Outline each Plasmodium ovale-infected red blood cell.
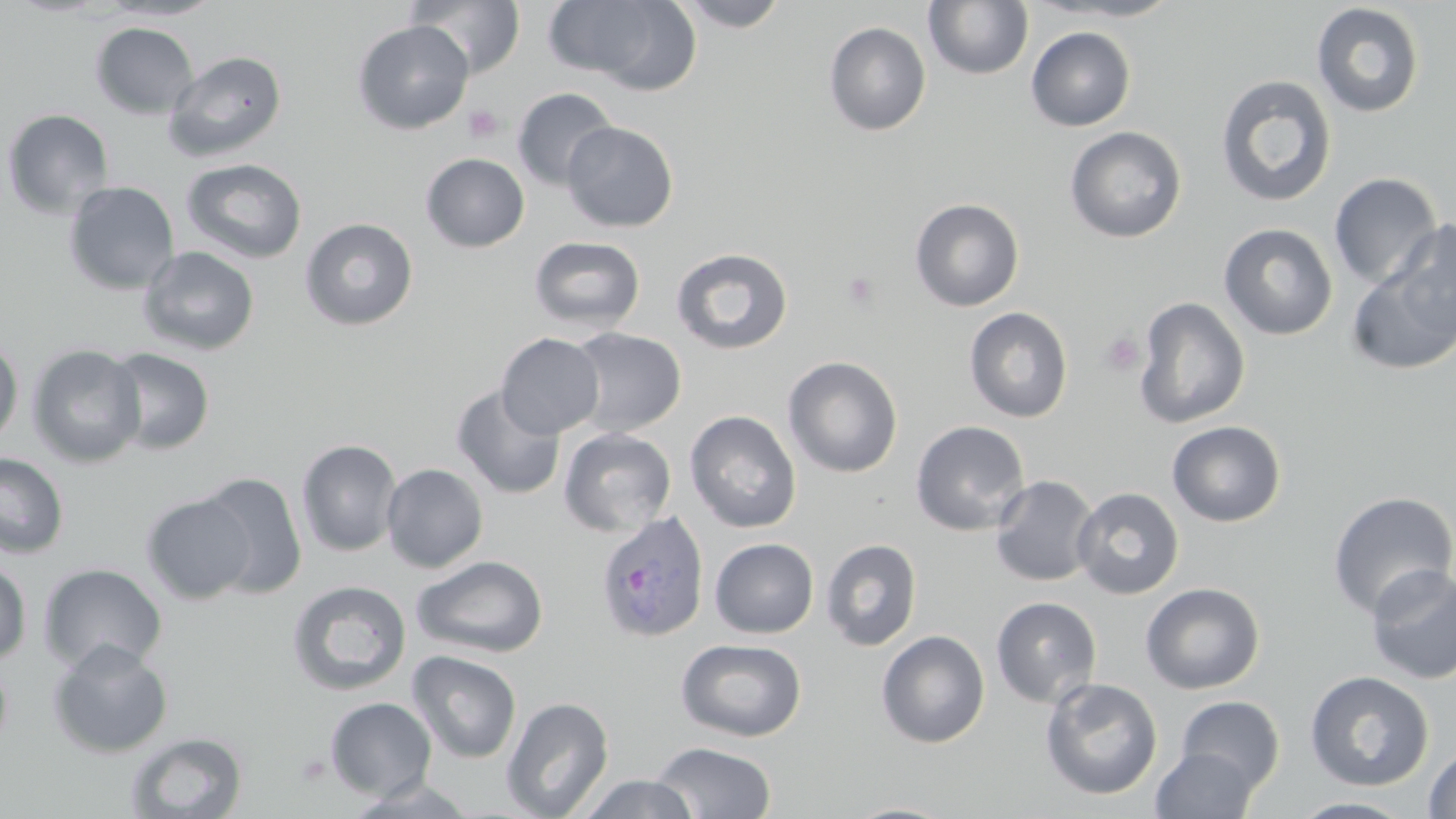
Approximate bounding boxes as named x1/y1/x2/y2 corners in pixels.
Plasmodium ovale-infected red blood cells: (x1=595, y1=510, x2=710, y2=643).

slide-level diagnosis = Plasmodium ovale
image size = 1456×819 pixels
field of view = one of a larger specimen
stain = May-Grünwald-Giemsa
magnification = 1000x
platelet locations = approximate bounding boxes as named x1/y1/x2/y2 corners in pixels: (x1=463, y1=105, x2=504, y2=144), (x1=840, y1=271, x2=883, y2=312), (x1=1099, y1=331, x2=1145, y2=376), (x1=293, y1=751, x2=332, y2=786)
modality = optical microscopy
uninfected red blood cell locations = approximate bounding boxes as named x1/y1/x2/y2 corners in pixels: (x1=101, y1=0, x2=225, y2=21), (x1=407, y1=0, x2=526, y2=79), (x1=544, y1=0, x2=700, y2=91), (x1=674, y1=0, x2=790, y2=31), (x1=923, y1=0, x2=1035, y2=80), (x1=1033, y1=0, x2=1187, y2=22), (x1=1311, y1=3, x2=1425, y2=118), (x1=352, y1=20, x2=474, y2=135), (x1=823, y1=21, x2=931, y2=136), (x1=90, y1=22, x2=199, y2=120), (x1=1025, y1=26, x2=1136, y2=131), (x1=163, y1=50, x2=288, y2=161), (x1=1215, y1=74, x2=1337, y2=207), (x1=512, y1=88, x2=618, y2=191), (x1=2, y1=108, x2=115, y2=220), (x1=561, y1=121, x2=679, y2=232), (x1=1065, y1=126, x2=1187, y2=243), (x1=421, y1=153, x2=530, y2=253), (x1=181, y1=158, x2=307, y2=264), (x1=1329, y1=172, x2=1443, y2=291), (x1=63, y1=181, x2=179, y2=295), (x1=910, y1=198, x2=1025, y2=311), (x1=1368, y1=216, x2=1455, y2=368), (x1=299, y1=218, x2=419, y2=331), (x1=1219, y1=223, x2=1338, y2=340), (x1=528, y1=235, x2=646, y2=334), (x1=137, y1=245, x2=260, y2=356), (x1=671, y1=247, x2=794, y2=355), (x1=1133, y1=296, x2=1250, y2=429), (x1=964, y1=307, x2=1073, y2=423), (x1=566, y1=327, x2=687, y2=437), (x1=496, y1=333, x2=605, y2=439), (x1=0, y1=337, x2=23, y2=449), (x1=27, y1=344, x2=146, y2=468), (x1=104, y1=347, x2=216, y2=456), (x1=783, y1=356, x2=903, y2=478), (x1=451, y1=385, x2=566, y2=500), (x1=684, y1=410, x2=802, y2=533), (x1=910, y1=420, x2=1030, y2=536), (x1=1167, y1=420, x2=1286, y2=528), (x1=558, y1=427, x2=677, y2=537), (x1=296, y1=439, x2=403, y2=557), (x1=0, y1=452, x2=69, y2=559), (x1=381, y1=462, x2=488, y2=573), (x1=196, y1=470, x2=308, y2=598), (x1=989, y1=475, x2=1100, y2=587), (x1=1071, y1=487, x2=1184, y2=599), (x1=1327, y1=491, x2=1456, y2=619), (x1=141, y1=493, x2=256, y2=604), (x1=709, y1=538, x2=819, y2=638), (x1=821, y1=539, x2=922, y2=652), (x1=411, y1=554, x2=549, y2=658), (x1=0, y1=557, x2=32, y2=664), (x1=39, y1=563, x2=168, y2=674), (x1=1365, y1=565, x2=1456, y2=685), (x1=287, y1=579, x2=412, y2=696), (x1=1140, y1=582, x2=1265, y2=695), (x1=990, y1=596, x2=1103, y2=708), (x1=876, y1=629, x2=990, y2=748), (x1=675, y1=638, x2=808, y2=742), (x1=47, y1=640, x2=174, y2=759), (x1=406, y1=650, x2=522, y2=763), (x1=0, y1=653, x2=13, y2=758), (x1=1304, y1=670, x2=1434, y2=791), (x1=1039, y1=677, x2=1164, y2=801), (x1=1175, y1=695, x2=1286, y2=794), (x1=502, y1=696, x2=614, y2=818), (x1=324, y1=697, x2=437, y2=801), (x1=125, y1=731, x2=248, y2=818), (x1=649, y1=741, x2=777, y2=819), (x1=1422, y1=746, x2=1456, y2=818), (x1=1150, y1=747, x2=1259, y2=819), (x1=578, y1=773, x2=698, y2=818), (x1=343, y1=778, x2=480, y2=817), (x1=1290, y1=796, x2=1417, y2=818), (x1=841, y1=801, x2=960, y2=819)
preparation = thin blood film